Assess this cell for malaria.
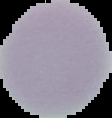

Uninfected.

Image is 112×118 pixels. Cell region segmented out of the field of view; the surrounding area is masked to black. From a thin blood film.